Locate every leukocyte (white blood cell).
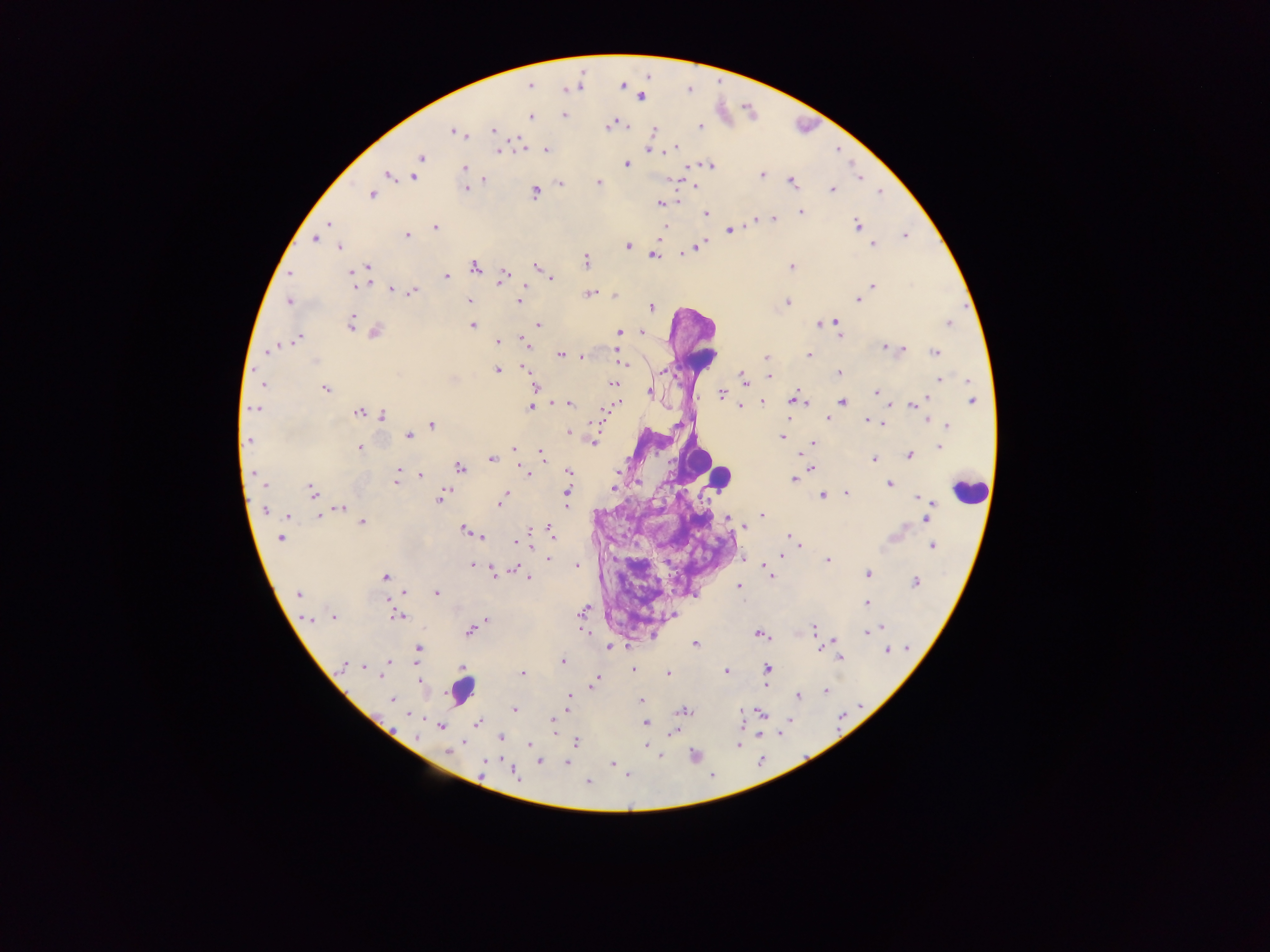
Approximate centers as (x, y) in pixels.
Leukocytes: (701, 356), (696, 458), (716, 477), (971, 490), (462, 688).

Plasmodium parasite locations: (529, 85), (640, 97), (564, 115), (530, 116), (611, 126), (701, 126), (494, 130), (454, 131), (654, 131), (519, 141), (675, 148), (498, 150), (546, 150), (648, 150), (421, 157), (626, 164), (710, 166), (464, 168), (389, 175), (762, 176), (415, 177), (484, 180), (598, 182), (560, 183), (792, 183), (466, 189), (832, 190), (535, 193), (372, 195), (661, 203), (801, 212), (706, 214), (777, 218), (772, 220), (755, 221), (328, 223), (858, 225), (435, 227), (663, 228), (730, 231), (407, 236), (905, 236), (315, 239), (873, 245), (627, 246), (697, 246), (339, 247), (693, 249), (654, 256), (586, 261), (536, 266), (792, 266), (367, 267), (475, 267), (362, 269), (290, 273), (353, 275), (446, 277), (503, 277), (551, 278), (356, 285), (871, 286), (392, 290), (412, 292), (588, 294), (614, 296), (858, 300), (470, 301), (519, 301), (289, 302), (787, 303), (652, 307), (836, 322), (820, 323), (948, 323), (350, 324), (472, 325), (539, 325), (376, 332), (619, 332), (642, 332), (839, 333), (299, 338), (523, 341), (497, 343), (885, 348), (899, 349), (268, 350), (935, 352), (560, 355), (619, 355), (808, 355), (582, 357), (765, 357), (315, 361), (624, 363), (527, 369), (497, 370), (662, 371), (839, 373), (768, 377), (743, 378), (940, 380), (612, 383), (263, 384), (536, 386), (326, 389), (650, 392), (876, 393), (722, 394), (797, 400), (973, 401), (763, 402), (842, 403), (569, 404), (615, 404), (915, 404), (740, 406), (531, 407), (608, 408), (254, 409), (359, 413), (383, 415), (828, 419), (928, 419), (870, 421), (881, 422), (432, 425), (947, 426), (568, 432), (572, 433), (409, 435), (782, 437), (249, 440), (593, 442), (812, 443), (360, 447), (939, 447), (514, 449), (910, 454), (543, 456), (491, 459), (874, 459), (459, 468), (811, 468), (568, 471), (400, 472), (526, 473), (616, 473), (420, 475), (794, 480), (396, 481), (889, 484), (265, 485), (613, 488), (311, 491), (846, 493), (567, 494), (821, 495), (441, 497), (503, 497), (922, 499), (501, 503), (341, 508), (266, 511), (927, 512), (762, 515), (287, 516), (319, 517), (729, 518), (362, 522), (465, 529), (550, 532), (471, 533), (480, 537), (280, 539), (791, 539), (518, 541), (796, 542), (932, 546), (780, 556), (549, 558), (828, 560), (473, 565), (577, 566), (516, 569), (770, 571), (868, 573), (495, 574), (385, 577), (527, 577), (916, 582), (739, 586), (436, 593), (299, 594), (867, 603), (583, 610), (397, 616), (333, 617), (486, 622), (813, 629), (874, 629), (471, 630), (868, 631), (584, 632), (760, 634), (695, 643), (609, 648), (418, 649), (887, 651), (839, 657), (563, 661), (387, 664), (344, 665), (360, 667), (463, 669), (633, 669), (767, 669), (383, 671), (726, 671), (522, 673), (667, 673), (597, 678), (420, 681), (595, 682), (825, 691), (798, 696), (569, 698), (392, 699), (641, 700), (514, 710), (683, 711), (552, 721), (645, 722), (477, 723), (441, 726), (673, 733), (500, 738), (577, 742), (529, 744), (738, 745), (647, 746), (449, 751), (484, 762), (540, 762), (566, 763), (613, 764), (516, 773), (589, 782). Thick blood film. One field of view. Photographed through a microscope with a mobile-phone camera. Image is 1270×952 pixels. Sample from Ghana.